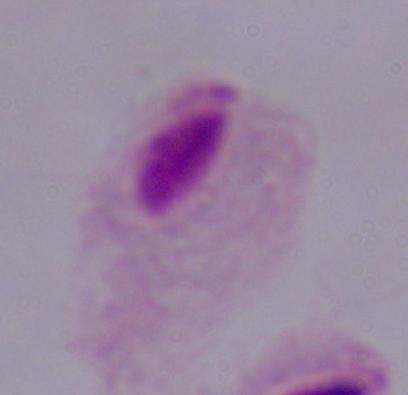

Summary:
  - Modality: micrograph
  - Identification: trichomonad
  - Magnification: 1000x